Report the malaria status of this cell.
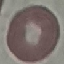

It is uninfected.

Thin blood film. Giemsa stain. Photographed with a smartphone camera at the microscope eyepiece. Cell patch, automatically extracted from a larger field of view and resized to 64 × 64 pixels.